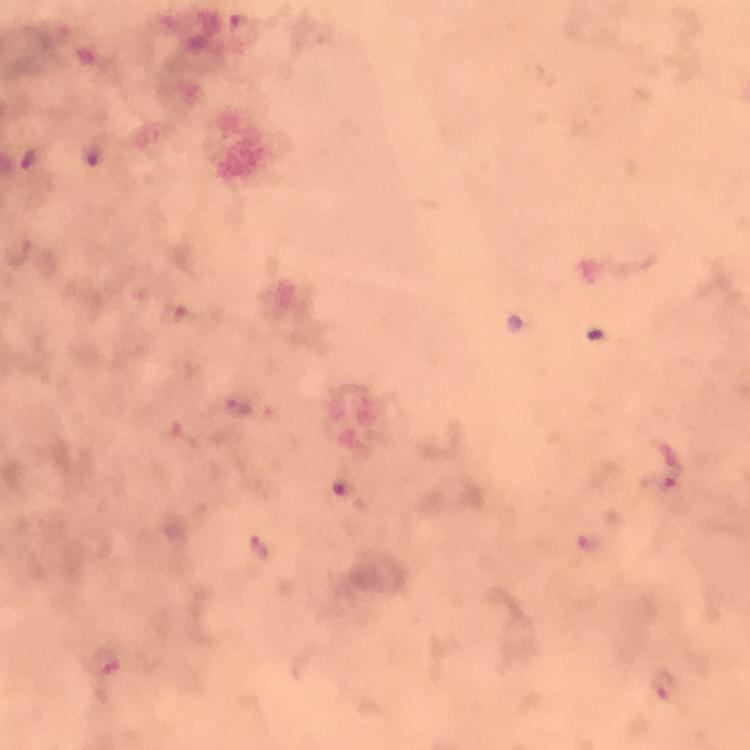
context = from a malaria diagnostic workup
image size = 750×750 pixels
preparation = thick smear
immersion oil = applied
stain = Giemsa
cropped from = one field of view
magnification = 100x
Plasmodium parasite locations = approximate centers as {x, y} in pixels: {667, 469}, {105, 662}, {664, 687}
capture = smartphone photograph through a microscope